Report the malaria status of this cell.
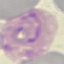
Parasitized.

Cell patch, automatically extracted from a larger field of view and resized to 64 × 64 pixels. Acquired by smartphone through the microscope eyepiece. Giemsa-stained preparation. Thin blood film.